Classify this cell by malaria status.
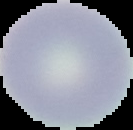
Uninfected.

preparation: thin blood smear
image_type: segmented cell region on a black background
image_size: 133×130 pixels